Report the malaria status of this cell.
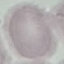
It is uninfected.

Cell patch, automatically extracted from a larger field of view and resized to 64 × 64 pixels. Thin blood film. Giemsa stain. Acquired by smartphone through the microscope eyepiece.